Name the blood parasite species.
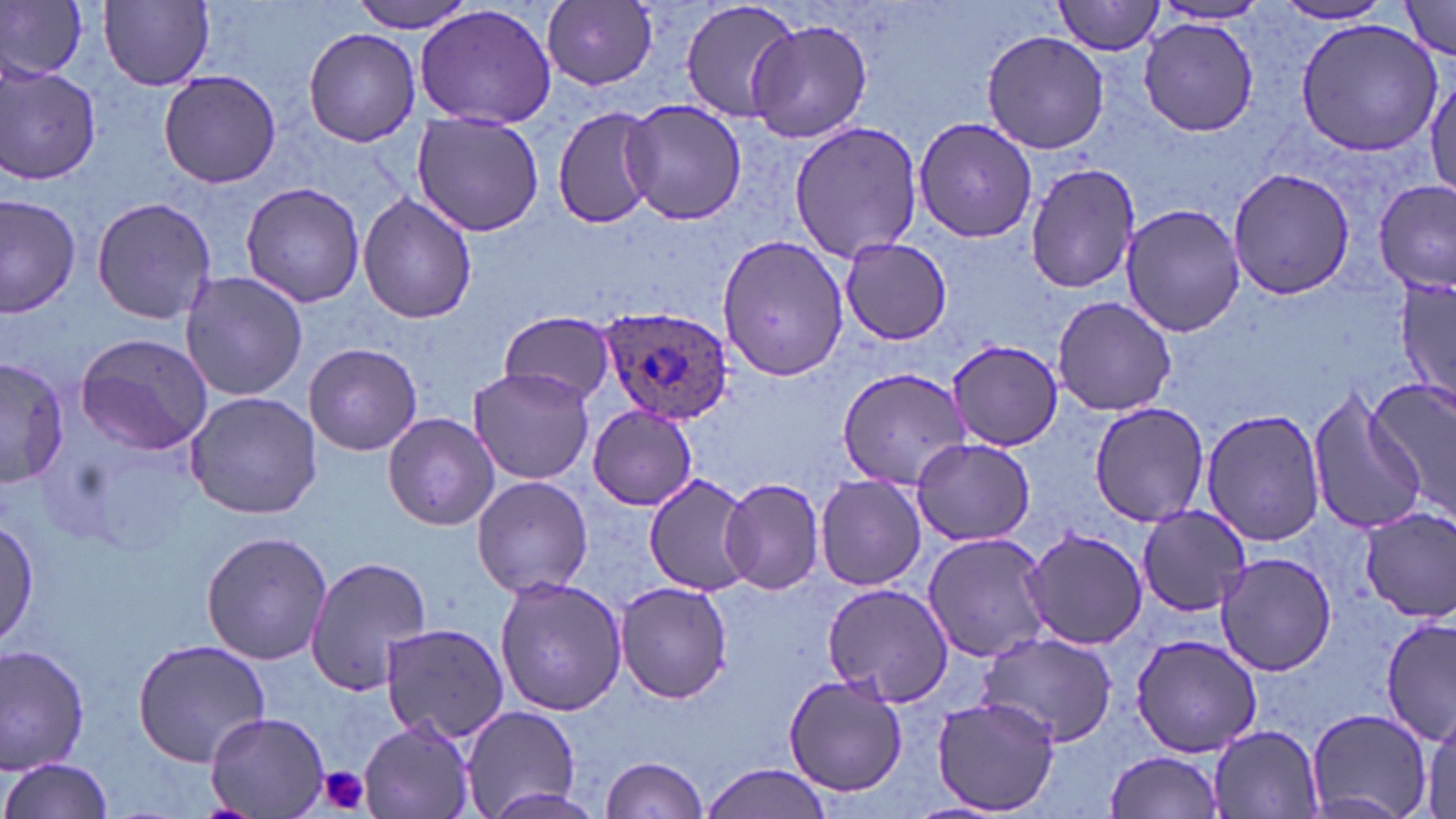

Plasmodium ovale.

magnification = 1000x
platelet locations = approximate bounding boxes as (x1,y1)-(x2,y2) corner pairs in pixels: (315,764)-(374,817)
preparation = thin blood film
uninfected red blood cell locations = approximate bounding boxes as (x1,y1)-(x2,y2) corner pairs in pixels: (101,0)-(215,89), (350,0)-(480,34), (680,0)-(807,125), (1054,0)-(1165,56), (0,1)-(87,81), (544,1)-(659,89), (1397,1)-(1456,60), (1275,2)-(1395,25), (414,3)-(557,130), (1153,3)-(1272,28), (1139,18)-(1259,135), (1296,19)-(1443,156), (747,20)-(872,144), (303,27)-(422,147), (984,30)-(1108,155), (1,63)-(101,186), (158,69)-(282,190), (1426,69)-(1456,198), (621,99)-(746,226), (551,104)-(662,230), (411,111)-(547,237), (912,115)-(1037,243), (788,121)-(921,263), (1023,162)-(1139,294), (1227,167)-(1358,299), (239,181)-(367,310), (1374,182)-(1454,294), (1,192)-(81,318), (357,192)-(478,324), (91,195)-(217,325), (1120,204)-(1245,338), (716,232)-(848,383), (837,236)-(955,345), (180,270)-(308,401), (1397,270)-(1454,409), (1051,294)-(1176,419), (499,310)-(615,406), (75,332)-(214,456), (946,338)-(1063,451), (303,342)-(424,456), (0,354)-(69,492), (467,366)-(594,485), (839,366)-(970,486), (1365,381)-(1456,515), (1307,385)-(1427,537), (185,391)-(323,520), (1087,399)-(1209,527), (585,403)-(698,510), (1202,408)-(1330,546), (383,412)-(499,531), (909,437)-(1036,547), (645,472)-(762,597), (471,475)-(593,599), (814,475)-(927,592), (722,476)-(827,597), (1135,504)-(1250,616), (1360,508)-(1456,625), (0,514)-(40,646), (1021,527)-(1148,650), (199,531)-(333,666), (922,532)-(1055,663), (1217,551)-(1340,676), (304,554)-(433,695), (493,575)-(627,718), (614,579)-(736,703), (819,581)-(956,707), (1380,615)-(1455,747), (378,622)-(513,745), (976,631)-(1121,748), (1130,635)-(1262,755), (132,638)-(271,766), (1,644)-(92,772), (782,675)-(909,798), (932,696)-(1059,815), (458,705)-(582,818), (1304,708)-(1435,819), (1424,709)-(1456,816), (205,712)-(330,816), (357,718)-(477,819), (1207,726)-(1326,817), (1105,750)-(1227,819), (599,756)-(710,818), (1,757)-(115,819), (698,762)-(835,819)
field of view = one of a larger specimen
image size = 1456×819 pixels
Plasmodium ovale-infected red blood cell locations = approximate bounding boxes as (x1,y1)-(x2,y2) corner pairs in pixels: (596,305)-(733,425)
stain = May-Grünwald-Giemsa
modality = optical microscopy